Point out every Plasmodium parasite.
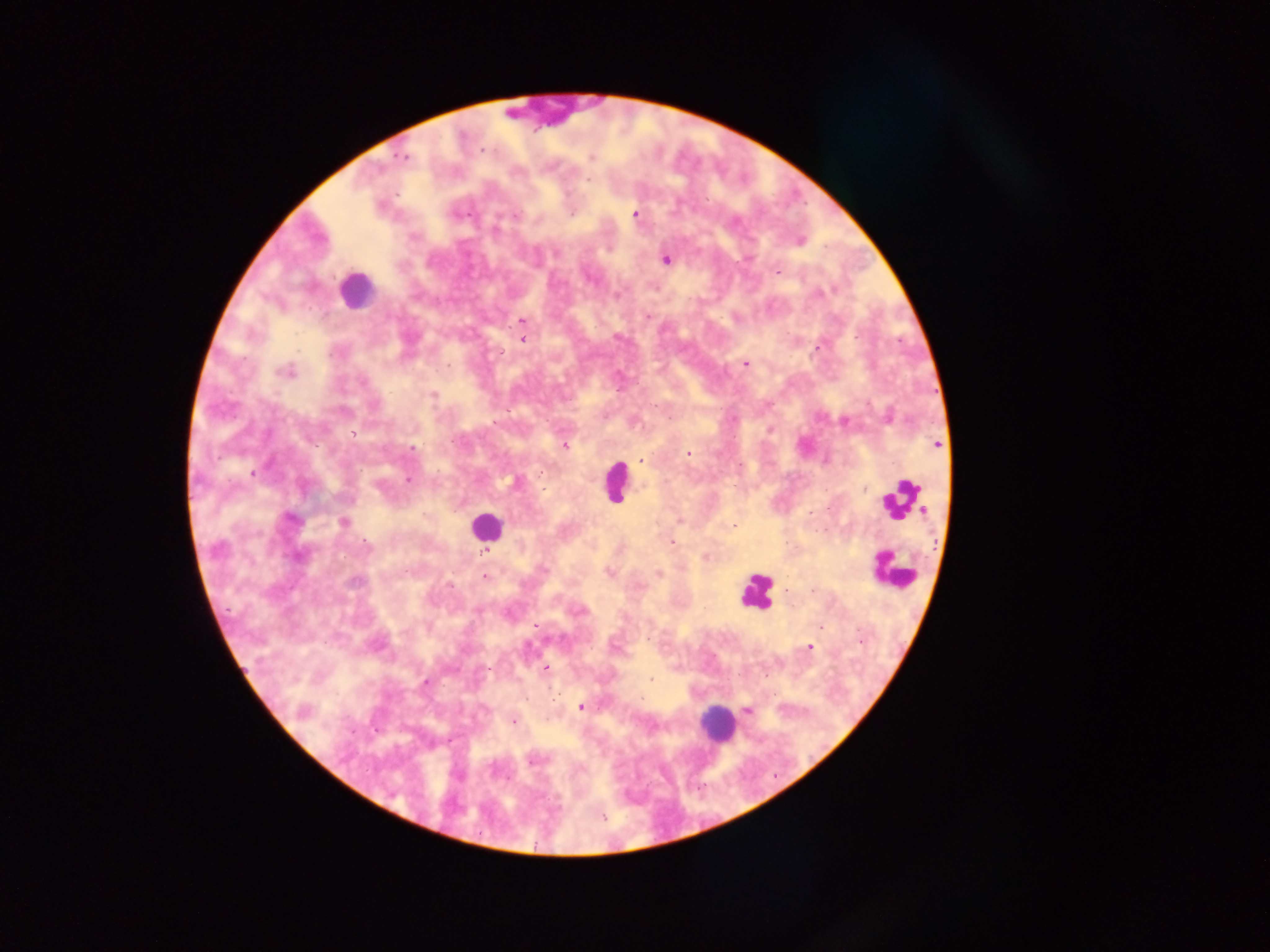

Approximate centers as [x, y] in pixels.
Plasmodium parasites: [481, 150], [591, 156], [403, 157], [590, 177], [636, 215], [800, 240], [666, 259], [778, 272], [648, 316], [523, 321], [522, 339], [745, 363], [286, 371], [433, 394], [889, 416], [845, 420], [495, 423], [564, 445], [937, 445], [411, 449], [687, 454], [639, 460], [408, 479], [516, 482], [342, 523], [733, 526], [672, 542], [706, 557], [608, 571], [659, 574], [485, 576], [788, 590], [536, 625], [809, 646], [545, 667], [487, 669], [651, 680], [581, 707], [747, 710], [513, 721], [603, 817].

{
  "image_size": "1270×952 pixels",
  "country": "Ghana",
  "field_of_view": "single",
  "capture": "mobile-phone photograph through a microscope",
  "leukocyte_locations": "approximate centers as [x, y] in pixels: [354, 290], [615, 483], [901, 500], [485, 527], [893, 569], [757, 592], [717, 724]",
  "preparation": "thick blood smear"
}